Give the position of every leukocyte visible.
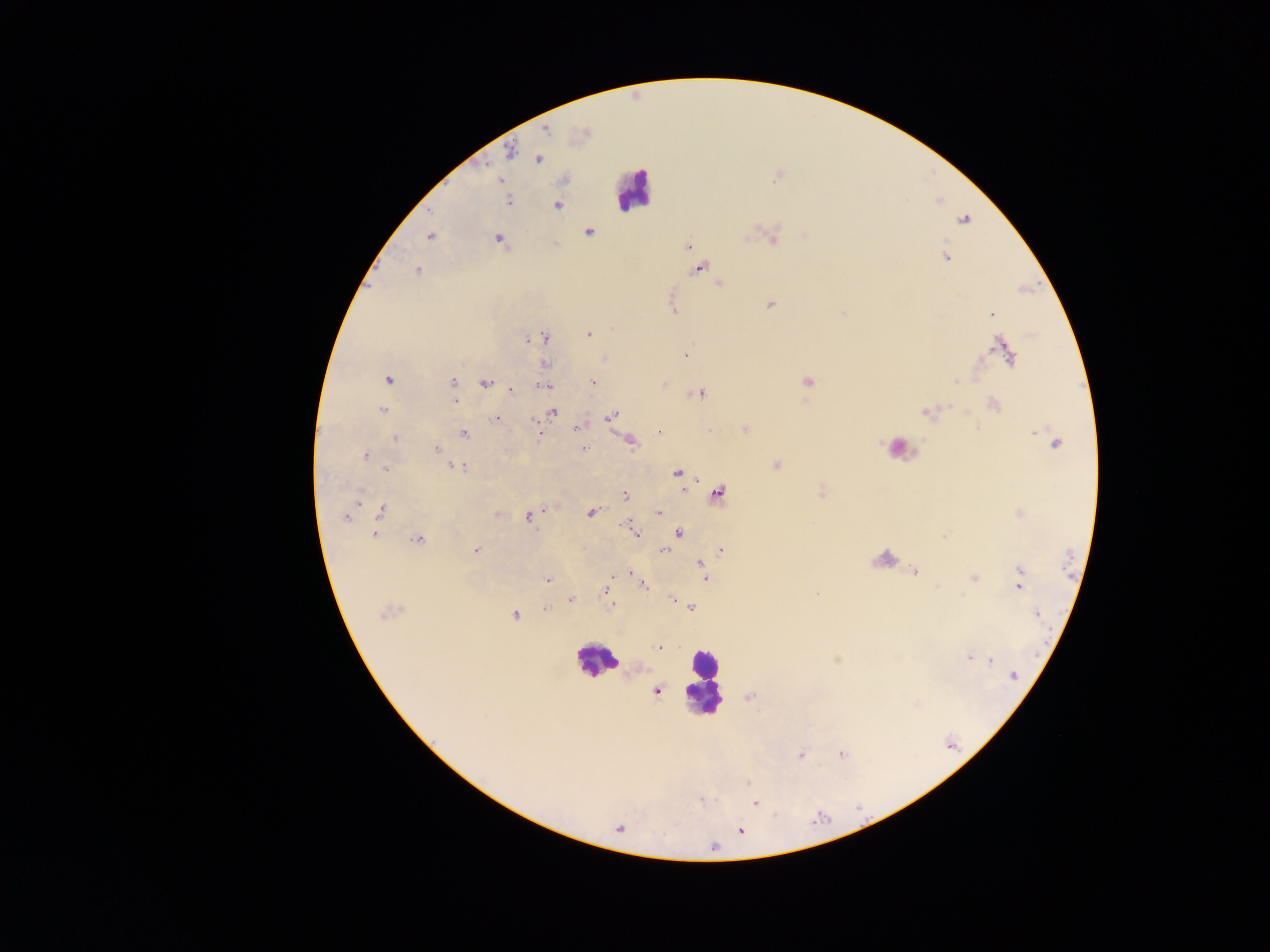
Approximate centers as [x, y] in pixels.
Leukocytes: [632, 189], [899, 448], [884, 560], [596, 661], [704, 682].

capture = mobile-phone photograph through a microscope
preparation = thick blood film
image size = 1270×952 pixels
country = Ghana
field of view = single
malaria parasite locations = approximate centers as [x, y] in pixels: [545, 129], [510, 151], [539, 160], [500, 180], [509, 201], [557, 206], [964, 220], [589, 232], [430, 236], [773, 238], [499, 240], [688, 246], [946, 257], [699, 268], [416, 270], [719, 284], [771, 304], [673, 306], [991, 314], [589, 334], [544, 338], [528, 339], [1005, 350], [685, 355], [604, 360], [545, 365], [387, 380], [956, 381], [593, 382], [807, 382], [453, 383], [485, 383], [544, 386], [511, 390], [701, 394], [455, 401], [993, 404], [382, 411], [553, 412], [924, 413], [613, 416], [496, 419], [578, 428], [746, 430], [659, 432], [464, 434], [539, 435], [395, 438], [631, 442], [1055, 442], [436, 449], [583, 449], [366, 455], [776, 465], [459, 467], [385, 469], [677, 473], [625, 494], [719, 494], [381, 509], [591, 512], [659, 513], [498, 514], [346, 516], [528, 517], [626, 526], [679, 533], [374, 534], [635, 534], [417, 540], [476, 550], [722, 550], [665, 551], [699, 565], [703, 572], [914, 572], [631, 573], [973, 578], [548, 579], [1019, 581], [643, 584], [605, 591], [817, 593], [570, 600], [673, 600], [611, 604], [692, 607], [545, 609], [1039, 614], [514, 615], [660, 647], [969, 657], [981, 658], [990, 660], [1014, 676], [656, 691], [841, 754], [801, 755], [747, 783], [700, 800], [755, 803], [741, 831], [714, 848]